Classify the preparation.
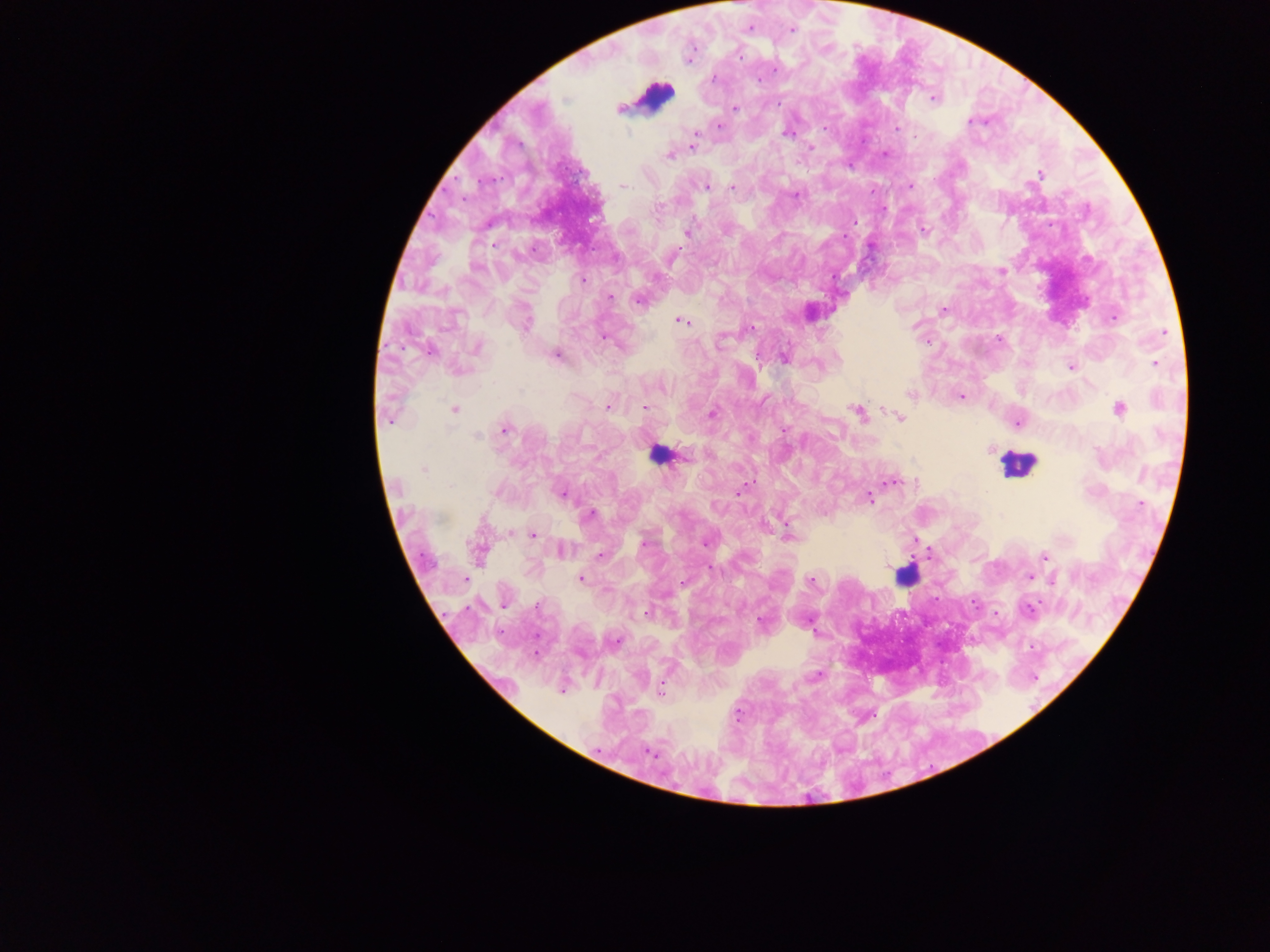
This is a thick smear.

{
  "leukocyte_locations": "approximate centers as [x, y] in pixels: [656, 95], [657, 454], [1018, 465], [905, 576]",
  "field_of_view": "single",
  "country": "Ghana",
  "capture": "mobile-phone photograph through a microscope",
  "image_size": "1270×952 pixels",
  "plasmodium_parasite_locations": "approximate centers as [x, y] in pixels: [791, 30], [739, 56], [775, 70], [713, 79], [758, 80], [933, 98], [734, 108], [970, 121], [719, 127], [824, 128], [896, 128], [696, 133], [787, 134], [915, 136], [692, 147], [811, 147], [885, 154], [669, 157], [1039, 174], [623, 186], [707, 187], [733, 187], [910, 187], [795, 197], [658, 208], [923, 229], [686, 233], [494, 244], [1001, 271], [583, 280], [610, 297], [638, 301], [943, 311], [1114, 318], [682, 321], [526, 324], [751, 327], [1165, 332], [604, 337], [999, 339], [926, 342], [478, 347], [430, 352], [557, 354], [784, 357], [1154, 363], [1070, 367], [460, 370], [661, 389], [910, 395], [961, 396], [607, 406], [644, 407], [1119, 408], [454, 410], [858, 413], [713, 414], [900, 417], [390, 420], [1018, 423], [506, 429], [784, 429], [478, 437], [990, 450], [686, 456], [423, 469], [891, 482], [745, 486], [450, 487], [741, 490], [561, 494], [869, 499], [1141, 504], [590, 515], [510, 533], [788, 533], [533, 534], [705, 543], [643, 544], [562, 550], [600, 555], [1045, 556], [1030, 577], [581, 578], [465, 580], [811, 580], [1054, 580], [682, 582], [538, 605], [1027, 611], [646, 613], [762, 621], [617, 642], [660, 690], [562, 691], [738, 714], [650, 753]"
}